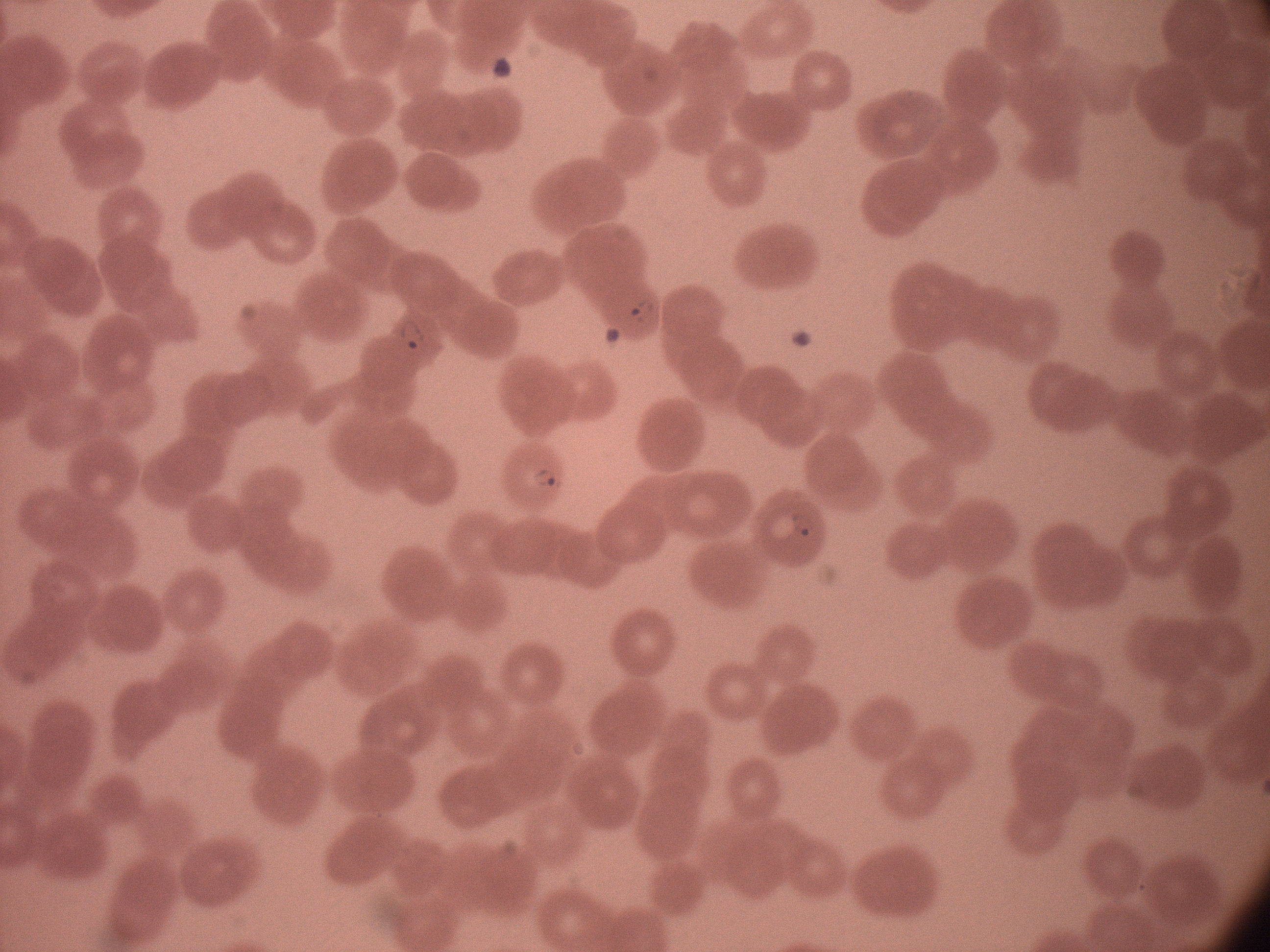
Approximate bounding boxes as named x1/y1/x2/y2 corners in pixels, from the source annotation, which is not necessarily exhaustive.
Summary:
  - Ring form locations: (x1=624, y1=292, x2=661, y2=325), (x1=395, y1=315, x2=429, y2=354), (x1=526, y1=462, x2=567, y2=492), (x1=782, y1=501, x2=820, y2=547)
  - Field of view: single
  - Magnification: 100x
  - Species: Plasmodium falciparum
  - Preparation: thin blood smear
  - Stain: Giemsa
  - Image size: 1270×952 pixels
  - Microscope: Leica DM2000 with built-in camera